Point out each Plasmodium parasite.
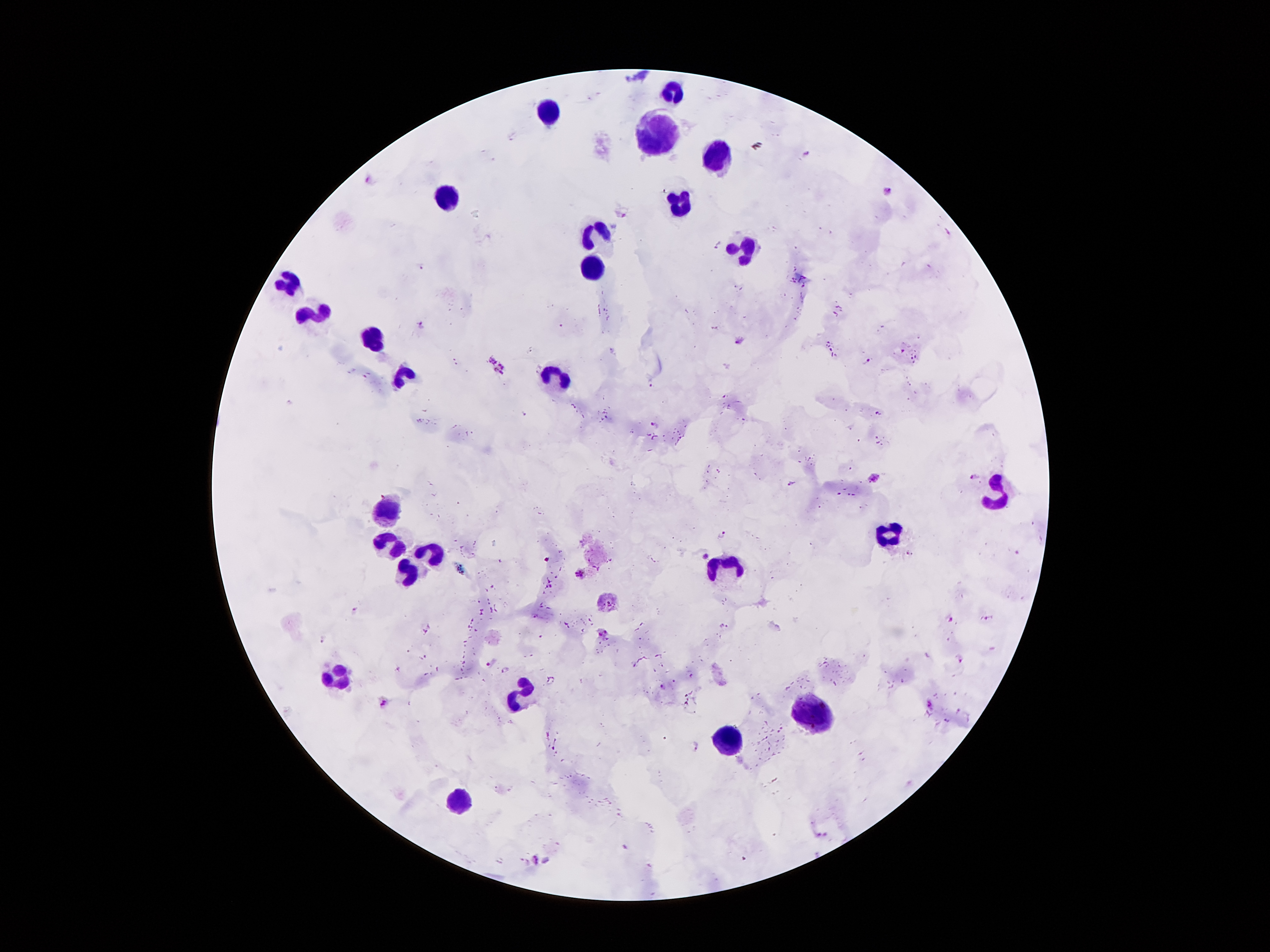

Approximate centers as {x, y} in pixels.
Plasmodium parasites: {806, 156}, {369, 179}, {889, 191}, {623, 210}, {946, 232}, {717, 243}, {421, 268}, {421, 325}, {740, 340}, {492, 360}, {868, 362}, {503, 367}, {499, 374}, {652, 385}, {655, 425}, {974, 478}, {874, 479}, {793, 482}, {725, 534}, {907, 553}, {705, 556}, {579, 573}, {985, 618}, {952, 621}, {603, 632}, {961, 660}, {504, 669}, {553, 681}, {663, 687}, {385, 702}, {930, 706}, {696, 748}, {822, 835}, {534, 859}.

Leukocyte locations: {673, 89}, {549, 112}, {659, 135}, {718, 163}, {447, 191}, {679, 199}, {598, 230}, {747, 248}, {595, 273}, {290, 284}, {319, 315}, {371, 337}, {554, 376}, {999, 494}, {387, 507}, {889, 537}, {390, 547}, {430, 554}, {725, 567}, {410, 570}, {339, 678}, {524, 694}, {815, 709}, {731, 737}, {462, 804}. Smartphone photograph taken through the microscope eyepiece. Patient malaria status: infected with Plasmodium falciparum. One field from this slide. 100x magnification. Image is 1270×952 pixels. Giemsa stain. Thick blood smear.